Assess this cell for malaria.
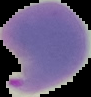

It is parasitized.

Image is 91×97 pixels. From a thin blood film. Segmented cell region on a black background.